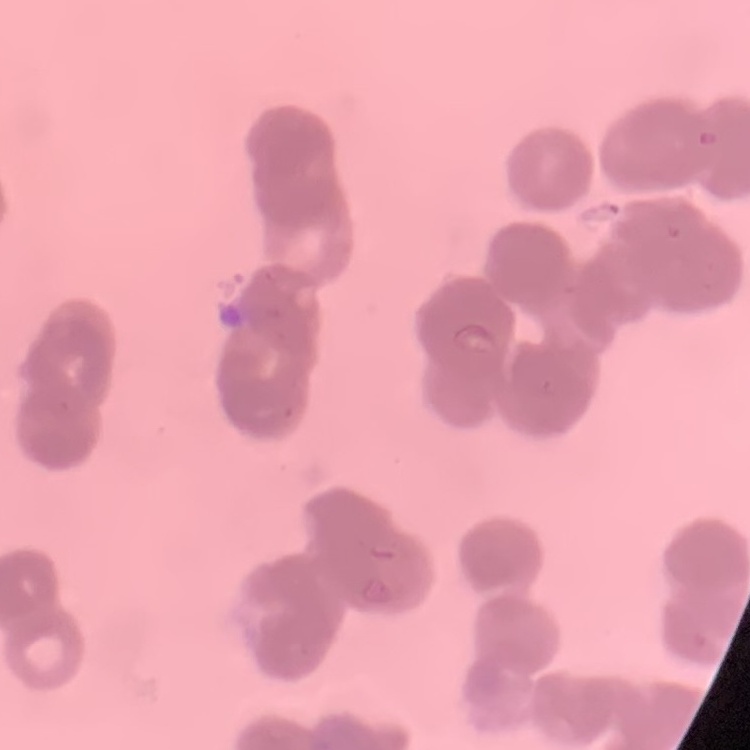

Summary:
  - Erythrocyte morphology: rouleaux formation
  - Stain: Field's or Giemsa
  - Image type: square crop of a larger photomicrograph
  - Preparation: thin blood smear